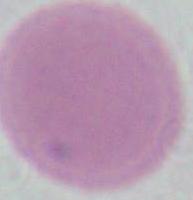
{
  "modality": "micrograph",
  "identification": "erythrocyte",
  "magnification": "1000x"
}